Report the malaria status.
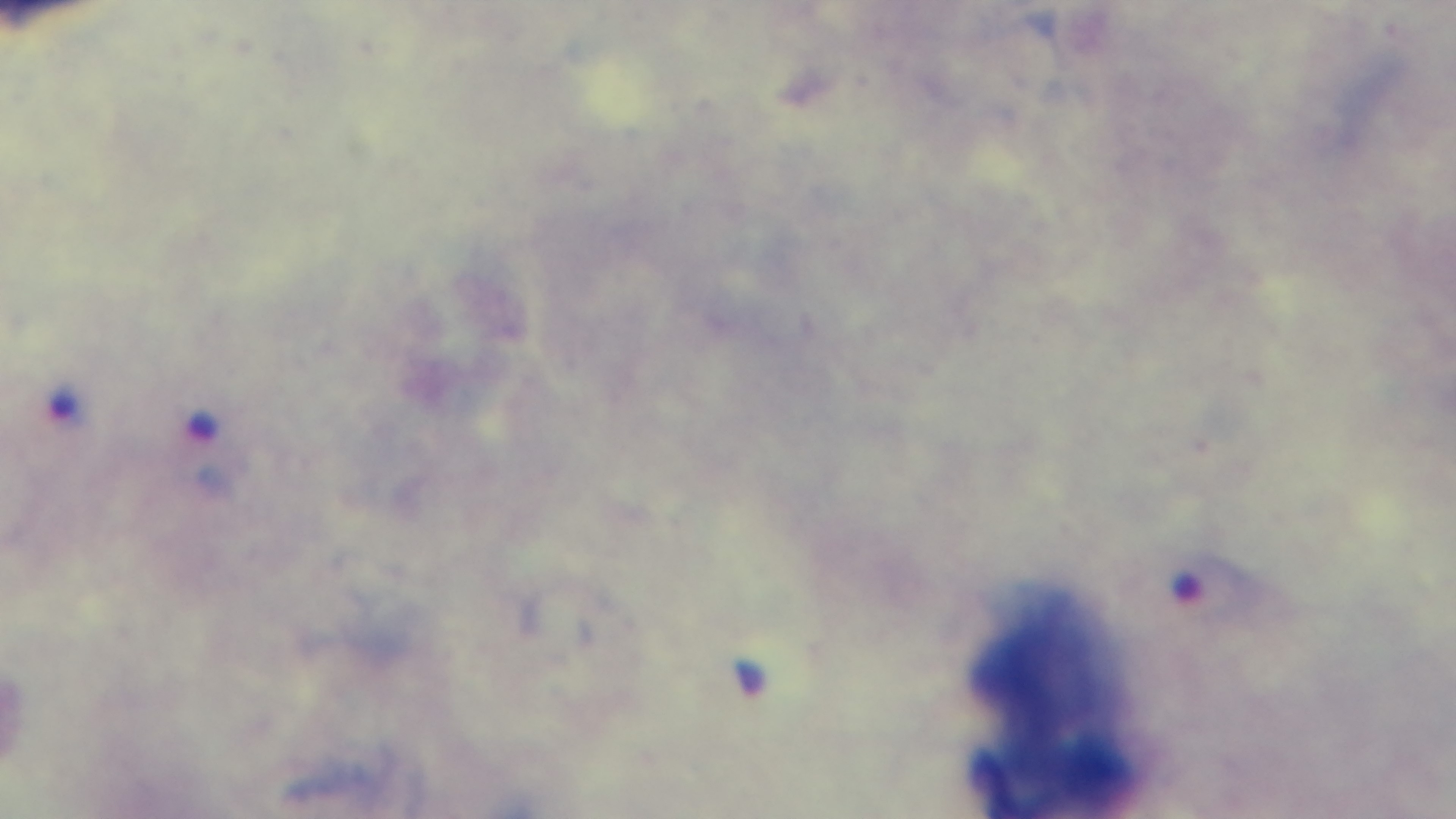
It is infected.

Summary:
  - Preparation: thick smear
  - Field of view: one from the slide
  - Capture: mounted 4K digital camera
  - Modality: light microscopy
  - Objective: 100x oil immersion
  - Stain: Giemsa